Assess this cell for malaria.
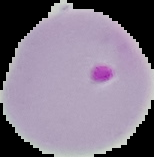

It is parasitized.

{
  "preparation": "thin blood film",
  "image_type": "cell region segmented out of the field of view; surrounding area masked to black",
  "image_size": "154×157 pixels"
}